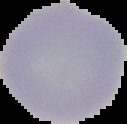

Summary:
  - Image type: segmented cell region with the area outside set to black
  - Preparation: thin blood smear
  - Malaria status: uninfected
  - Image size: 127×124 pixels